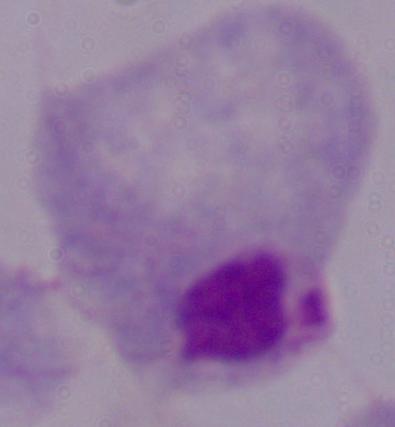 A trichomonad is seen. 1000x magnification. Micrograph.